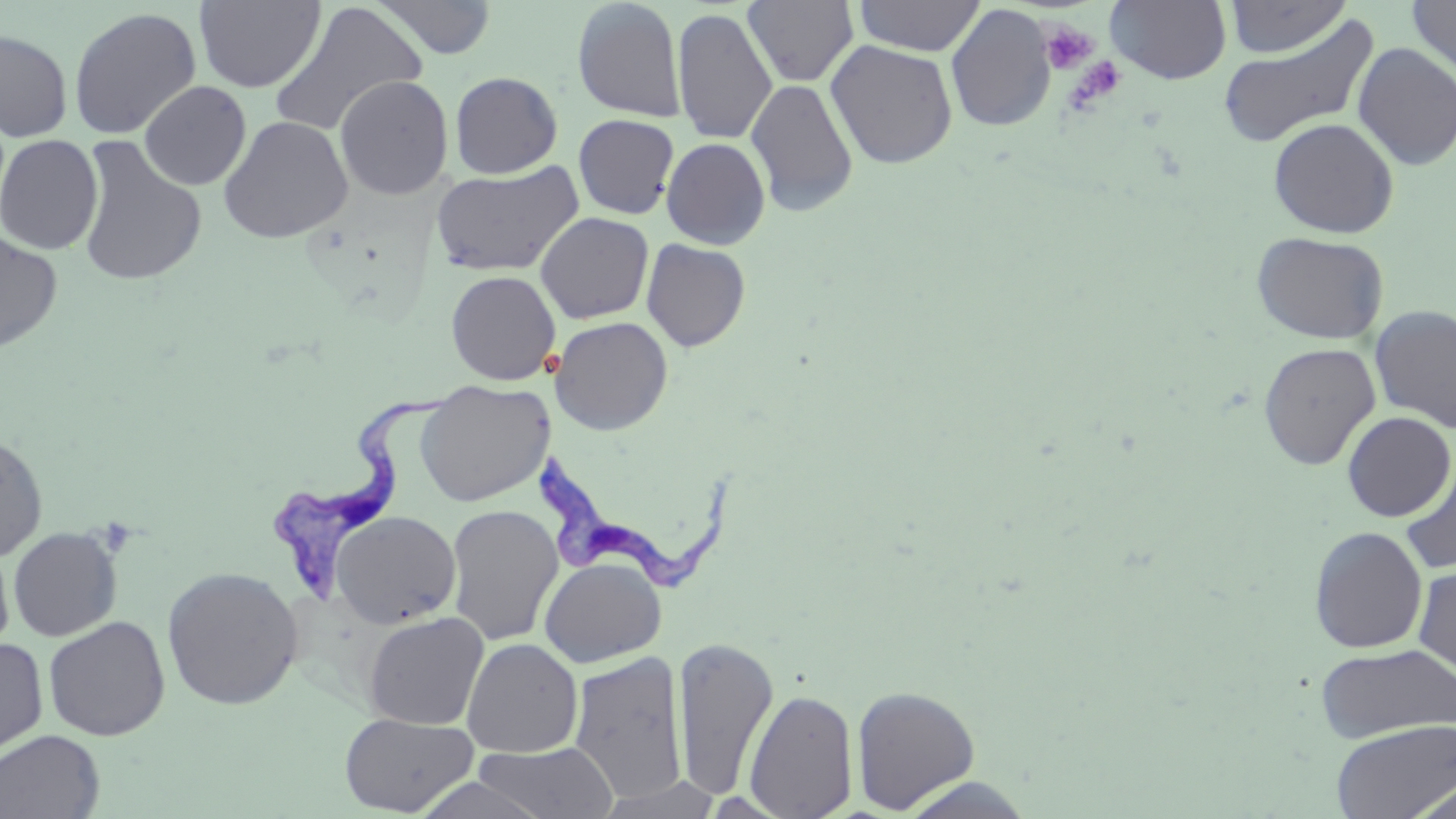

Approximate bounding boxes as (x1, y1, x2, y2) in pixels. Trypanosoma brucei locations: (267, 392, 449, 603), (539, 455, 735, 594). Platelet locations: (1039, 20, 1098, 74), (1066, 56, 1126, 109). Uninfected red blood cell locations: (194, 0, 325, 92), (372, 0, 498, 60), (743, 0, 859, 88), (853, 0, 985, 56), (1105, 0, 1232, 84), (1223, 0, 1352, 58), (572, 1, 687, 122), (1407, 1, 1456, 83), (268, 2, 428, 139), (945, 4, 1057, 132), (68, 7, 202, 140), (672, 7, 777, 145), (1216, 13, 1381, 151), (0, 29, 73, 142), (825, 39, 958, 169), (1353, 42, 1456, 170), (450, 71, 562, 178), (334, 75, 454, 200), (746, 78, 859, 217), (139, 80, 251, 190), (573, 114, 679, 219), (218, 115, 354, 243), (1268, 118, 1399, 237), (0, 134, 103, 255), (74, 135, 207, 286), (661, 137, 770, 249), (431, 163, 584, 277), (536, 212, 654, 324), (0, 230, 63, 353), (1251, 231, 1390, 345), (641, 239, 751, 352), (445, 270, 561, 385), (1369, 305, 1456, 433), (550, 316, 673, 435), (1258, 342, 1380, 470), (416, 380, 553, 507), (1342, 412, 1455, 520), (0, 431, 49, 562), (1399, 458, 1456, 577), (445, 504, 564, 647), (329, 510, 461, 629), (8, 526, 123, 642), (1308, 526, 1428, 654), (0, 540, 15, 654), (539, 557, 666, 668), (1413, 563, 1456, 676), (161, 565, 304, 711), (363, 610, 489, 730), (43, 616, 170, 741), (672, 635, 779, 801), (0, 637, 49, 758), (461, 638, 583, 757), (1314, 642, 1456, 744), (568, 650, 690, 804), (851, 684, 980, 813), (743, 687, 859, 818), (338, 712, 478, 816), (1331, 719, 1456, 819), (0, 730, 105, 818), (471, 741, 620, 819), (413, 775, 550, 819), (896, 776, 1038, 818), (1402, 777, 1456, 819), (594, 779, 722, 818). Slide-level diagnosis: Trypanosoma brucei. Optical microscopy. One field of a larger specimen. Captured at 1000x magnification. May-Grünwald-Giemsa-stained preparation. Image is 1456×819 pixels. Thin blood film.